Locate every Plasmodium ovale-infected red blood cell.
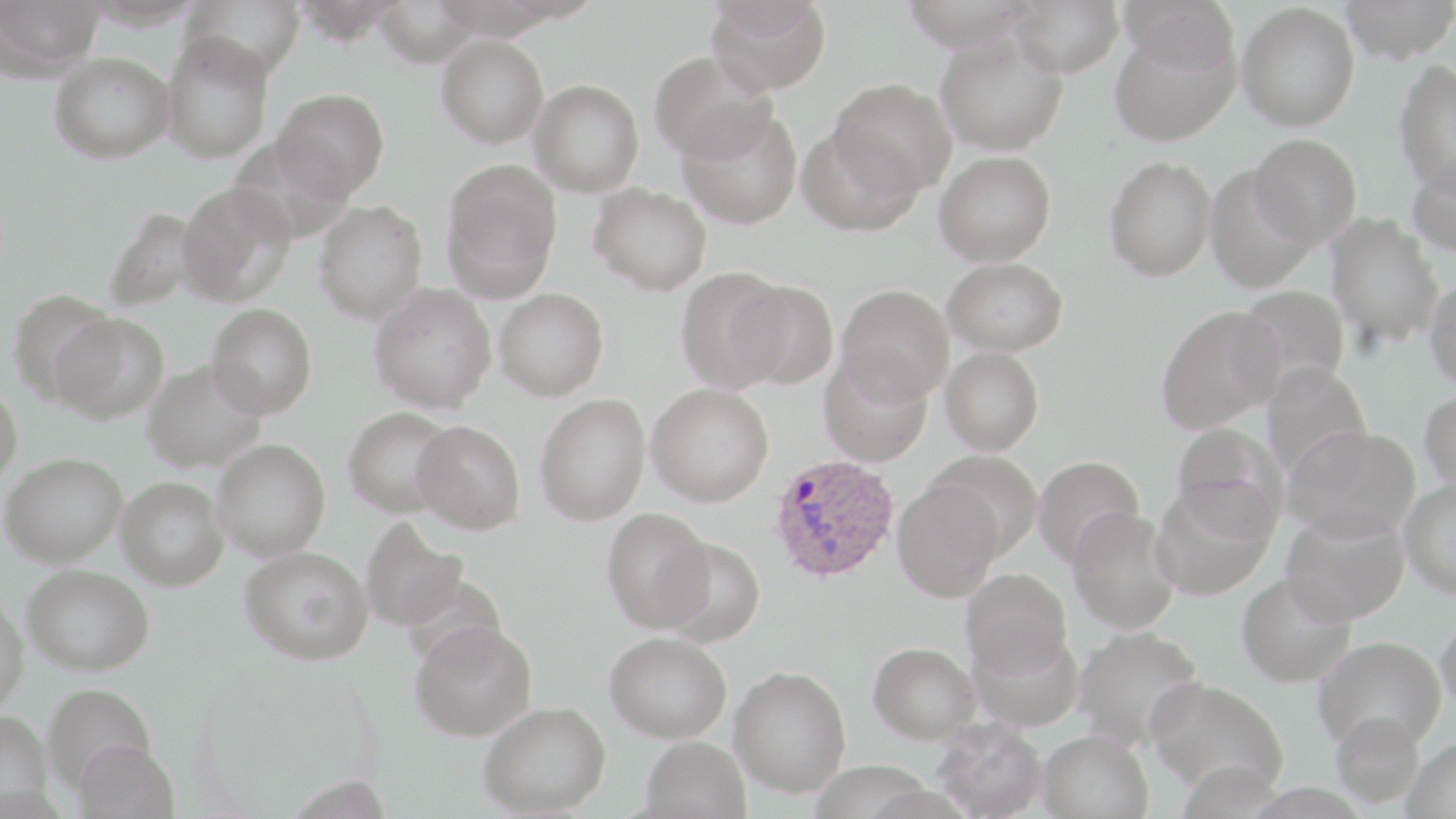

Approximate bounding boxes as named x1/y1/x2/y2 corners in pixels.
Plasmodium ovale-infected red blood cells: (x1=769, y1=453, x2=899, y2=583).

Summary:
  - Uninfected red blood cell locations: (x1=0, y1=0, x2=103, y2=78), (x1=183, y1=0, x2=303, y2=80), (x1=706, y1=0, x2=831, y2=96), (x1=1007, y1=0, x2=1124, y2=78), (x1=1119, y1=0, x2=1239, y2=78), (x1=1338, y1=0, x2=1456, y2=64), (x1=371, y1=1, x2=483, y2=66), (x1=1236, y1=2, x2=1360, y2=131), (x1=1110, y1=25, x2=1240, y2=145), (x1=161, y1=31, x2=274, y2=163), (x1=936, y1=31, x2=1068, y2=156), (x1=436, y1=34, x2=549, y2=148), (x1=650, y1=50, x2=775, y2=164), (x1=49, y1=51, x2=174, y2=164), (x1=1393, y1=59, x2=1456, y2=196), (x1=828, y1=77, x2=957, y2=197), (x1=529, y1=79, x2=645, y2=198), (x1=273, y1=88, x2=390, y2=200), (x1=678, y1=106, x2=803, y2=230), (x1=798, y1=124, x2=924, y2=236), (x1=1249, y1=134, x2=1362, y2=247), (x1=934, y1=150, x2=1056, y2=266), (x1=1407, y1=151, x2=1456, y2=258), (x1=1104, y1=156, x2=1216, y2=282), (x1=442, y1=160, x2=563, y2=294), (x1=1204, y1=166, x2=1317, y2=293), (x1=176, y1=182, x2=295, y2=305), (x1=589, y1=183, x2=712, y2=295), (x1=314, y1=200, x2=428, y2=324), (x1=103, y1=206, x2=203, y2=312), (x1=1325, y1=213, x2=1444, y2=349), (x1=942, y1=257, x2=1068, y2=357), (x1=675, y1=267, x2=792, y2=392), (x1=732, y1=279, x2=839, y2=389), (x1=1424, y1=279, x2=1456, y2=393), (x1=369, y1=283, x2=497, y2=413), (x1=835, y1=284, x2=954, y2=404), (x1=1235, y1=285, x2=1351, y2=391), (x1=494, y1=288, x2=609, y2=400), (x1=6, y1=289, x2=118, y2=404), (x1=207, y1=303, x2=317, y2=418), (x1=1156, y1=305, x2=1284, y2=433), (x1=50, y1=312, x2=170, y2=424), (x1=940, y1=346, x2=1045, y2=456), (x1=818, y1=354, x2=932, y2=467), (x1=142, y1=360, x2=266, y2=472), (x1=1261, y1=362, x2=1371, y2=478), (x1=0, y1=381, x2=23, y2=485), (x1=646, y1=383, x2=774, y2=506), (x1=1419, y1=390, x2=1456, y2=493), (x1=535, y1=394, x2=651, y2=525), (x1=343, y1=407, x2=458, y2=518), (x1=412, y1=419, x2=525, y2=533), (x1=1171, y1=422, x2=1288, y2=534), (x1=1284, y1=424, x2=1421, y2=544), (x1=212, y1=438, x2=330, y2=561), (x1=930, y1=450, x2=1044, y2=559), (x1=1, y1=452, x2=127, y2=567), (x1=1032, y1=455, x2=1145, y2=567), (x1=116, y1=476, x2=229, y2=590), (x1=892, y1=477, x2=1005, y2=603), (x1=1398, y1=477, x2=1456, y2=598), (x1=1151, y1=480, x2=1277, y2=601), (x1=601, y1=508, x2=714, y2=633), (x1=1068, y1=508, x2=1180, y2=634), (x1=1281, y1=511, x2=1408, y2=626), (x1=361, y1=517, x2=468, y2=631), (x1=657, y1=536, x2=766, y2=646), (x1=240, y1=545, x2=374, y2=664), (x1=22, y1=563, x2=154, y2=675), (x1=961, y1=568, x2=1072, y2=677), (x1=1237, y1=572, x2=1356, y2=686), (x1=0, y1=592, x2=28, y2=715), (x1=1435, y1=608, x2=1456, y2=717), (x1=409, y1=620, x2=537, y2=741), (x1=1073, y1=625, x2=1205, y2=750), (x1=968, y1=626, x2=1084, y2=730), (x1=605, y1=632, x2=732, y2=743), (x1=1312, y1=636, x2=1446, y2=752), (x1=868, y1=642, x2=980, y2=742), (x1=729, y1=666, x2=851, y2=797), (x1=1146, y1=678, x2=1288, y2=798), (x1=41, y1=683, x2=156, y2=791), (x1=479, y1=701, x2=611, y2=817), (x1=0, y1=709, x2=52, y2=814), (x1=1331, y1=711, x2=1425, y2=807), (x1=933, y1=720, x2=1047, y2=819), (x1=1037, y1=729, x2=1154, y2=819), (x1=640, y1=736, x2=752, y2=819), (x1=1402, y1=737, x2=1456, y2=819), (x1=71, y1=740, x2=179, y2=818)
  - Slide-level diagnosis: Plasmodium ovale
  - Magnification: 1000x
  - Modality: optical microscopy
  - Stain: May-Grünwald-Giemsa
  - Preparation: thin blood film
  - Field of view: single
  - Image size: 1456×819 pixels